Assess this cell for malaria.
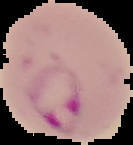

Parasitized.

Summary:
  - Preparation: thin blood smear
  - Image type: cell region segmented out of the field of view; surrounding area masked to black
  - Image size: 133×145 pixels